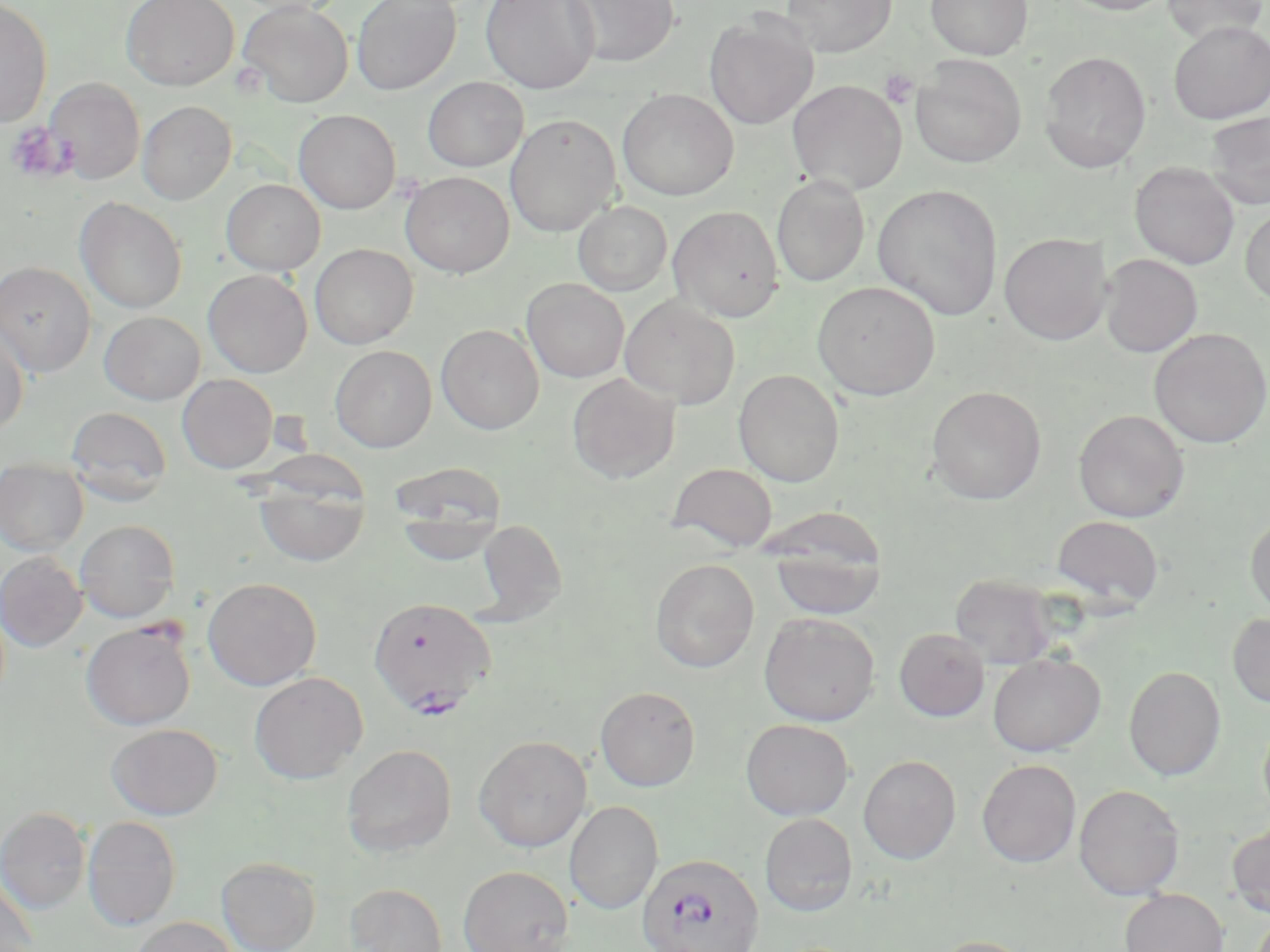

Summary:
  - Coordinate format: approximate bounding boxes as [x1, y1, x2, y2] in pixels
  - Uninfected red blood cell locations: [122, 0, 239, 91], [231, 0, 346, 17], [352, 0, 461, 95], [481, 0, 599, 94], [563, 0, 678, 67], [780, 0, 897, 58], [926, 0, 1033, 60], [1059, 0, 1176, 15], [1161, 0, 1268, 45], [0, 1, 53, 127], [238, 1, 353, 106], [704, 15, 819, 130], [1168, 21, 1270, 125], [1039, 51, 1152, 173], [910, 55, 1027, 168], [44, 77, 145, 185], [423, 77, 528, 172], [787, 79, 907, 195], [618, 89, 738, 200], [137, 101, 236, 204], [293, 109, 401, 214], [1204, 111, 1270, 210], [505, 114, 621, 237], [1129, 162, 1240, 269], [400, 171, 514, 277], [771, 174, 870, 287], [221, 179, 325, 275], [872, 183, 1004, 321], [75, 197, 187, 314], [573, 200, 672, 296], [668, 205, 785, 322], [1240, 206, 1270, 306], [999, 232, 1112, 345], [310, 243, 417, 349], [1100, 254, 1203, 358], [0, 261, 96, 377], [203, 269, 312, 377], [521, 278, 629, 382], [813, 281, 940, 399], [619, 296, 740, 408], [99, 311, 205, 404], [0, 322, 29, 436], [436, 324, 544, 434], [1149, 327, 1270, 448], [330, 345, 437, 451], [733, 369, 844, 487], [177, 373, 278, 473], [567, 373, 679, 483], [927, 386, 1046, 504], [66, 406, 171, 505], [1072, 409, 1190, 522], [0, 458, 89, 555], [389, 460, 507, 540], [667, 462, 778, 552], [253, 474, 371, 567], [1246, 514, 1270, 614], [1052, 515, 1163, 608], [476, 518, 567, 623], [75, 519, 180, 623], [765, 519, 888, 622], [0, 552, 87, 651], [650, 558, 759, 673], [950, 574, 1059, 668], [202, 577, 322, 690], [759, 612, 880, 726], [1227, 612, 1270, 708], [81, 621, 196, 730], [894, 628, 990, 722], [987, 652, 1106, 755], [1123, 665, 1226, 781], [249, 671, 368, 784], [595, 686, 701, 791], [1259, 714, 1270, 819], [740, 718, 854, 820], [106, 723, 223, 819], [474, 735, 592, 852], [342, 744, 457, 858], [858, 755, 961, 863], [977, 759, 1081, 868], [1073, 784, 1185, 900], [565, 801, 663, 914], [1, 807, 91, 914], [759, 813, 857, 916], [83, 816, 181, 930], [1226, 820, 1270, 919], [216, 857, 320, 952], [458, 865, 573, 952], [0, 875, 38, 952], [345, 882, 448, 952], [1120, 889, 1229, 952], [129, 916, 239, 952], [928, 935, 1039, 952]
  - Plasmodium falciparum-infected red blood cell locations: [368, 596, 496, 717], [636, 851, 765, 952]
  - Platelet locations: [879, 69, 918, 108], [5, 122, 70, 182]
  - Slide-level diagnosis: Plasmodium falciparum
  - Field of view: one of a larger specimen
  - Magnification: 1000x
  - Preparation: thin blood smear
  - Stain: May-Grünwald-Giemsa
  - Image size: 1270×952 pixels
  - Modality: light microscopy